Outline each Plasmodium malariae-infected red blood cell.
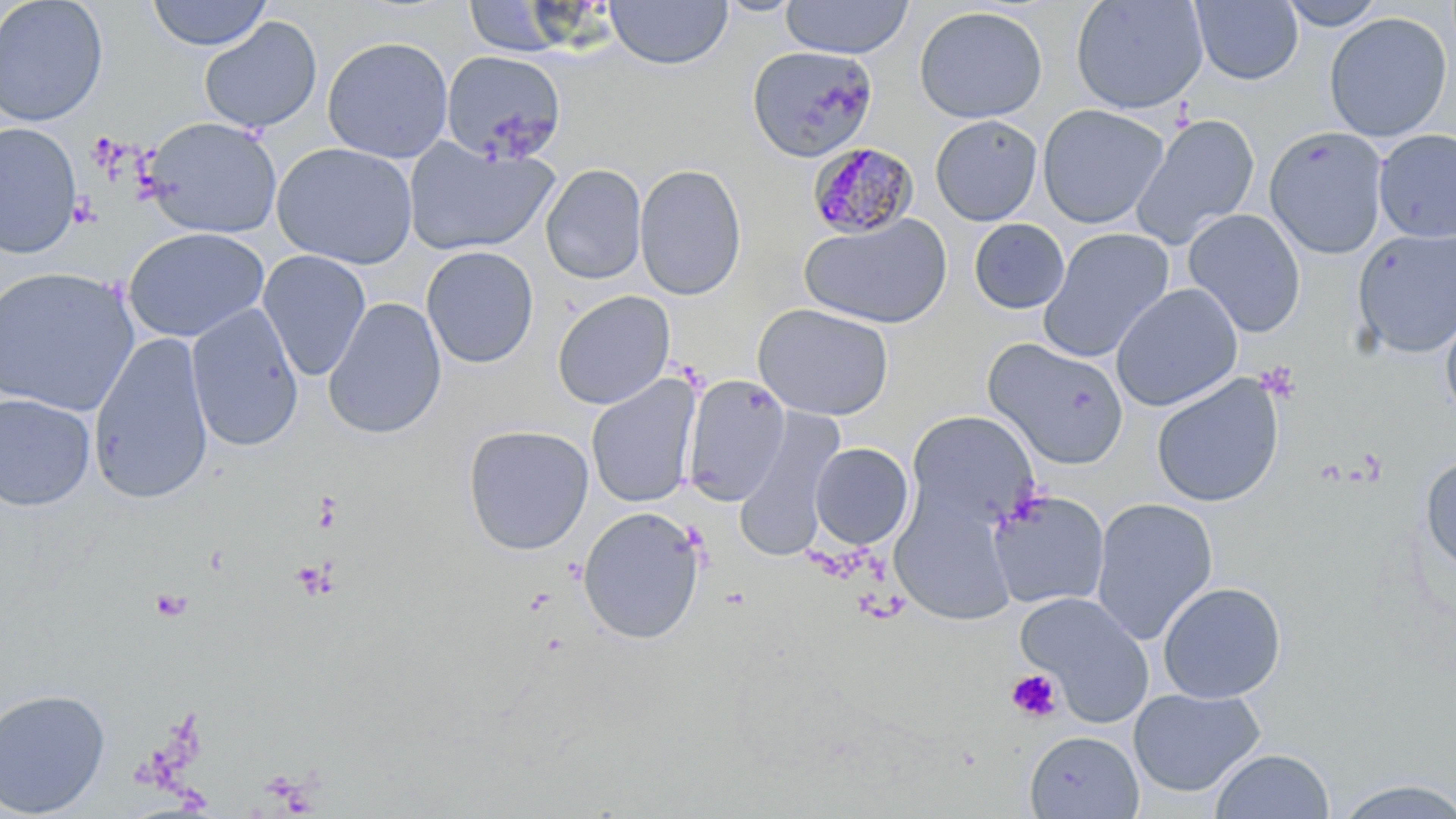

Approximate bounding boxes as [x1, y1, x2, y2] in pixels.
Plasmodium malariae-infected red blood cells: [807, 141, 918, 239].

slide-level diagnosis = Plasmodium malariae
modality = optical microscopy
stain = May-Grünwald-Giemsa
image size = 1456×819 pixels
uninfected red blood cell locations = approximate bounding boxes as [x1, y1, x2, y2] in pixels: [0, 0, 109, 127], [605, 0, 732, 69], [715, 0, 805, 17], [780, 0, 914, 59], [1070, 0, 1209, 114], [1190, 0, 1303, 85], [1277, 0, 1389, 30], [145, 1, 273, 51], [463, 1, 572, 57], [914, 5, 1048, 123], [1323, 12, 1453, 143], [198, 16, 323, 135], [321, 36, 454, 163], [747, 45, 878, 163], [440, 51, 567, 163], [1037, 104, 1170, 229], [1130, 113, 1260, 251], [930, 114, 1043, 226], [142, 116, 282, 239], [0, 122, 83, 259], [1265, 127, 1389, 259], [1373, 128, 1456, 244], [403, 138, 559, 256], [271, 143, 418, 269], [541, 163, 647, 285], [634, 163, 746, 300], [1183, 209, 1307, 337], [800, 213, 953, 329], [968, 219, 1070, 314], [123, 227, 270, 343], [1038, 227, 1175, 363], [1352, 228, 1456, 359], [421, 246, 539, 369], [258, 250, 371, 381], [0, 267, 141, 418], [1110, 282, 1242, 412], [551, 290, 676, 410], [323, 297, 447, 439], [186, 302, 304, 452], [752, 303, 894, 420], [1440, 303, 1456, 425], [88, 333, 214, 504], [983, 338, 1129, 470], [585, 374, 702, 509], [683, 374, 789, 505], [1150, 374, 1285, 508], [0, 393, 96, 511], [734, 407, 845, 563], [906, 409, 1040, 531], [462, 424, 594, 556], [810, 442, 913, 549], [1420, 454, 1456, 576], [988, 490, 1110, 610], [891, 493, 1016, 626], [1090, 496, 1218, 645], [577, 506, 706, 644], [1157, 581, 1286, 704], [1015, 591, 1154, 724], [1128, 687, 1266, 797], [0, 688, 112, 817], [1024, 730, 1144, 818], [1208, 748, 1335, 819], [1331, 777, 1456, 819]
platelet locations = approximate bounding boxes as [x1, y1, x2, y2] in pixels: [1257, 362, 1301, 402], [312, 493, 342, 533], [290, 559, 337, 601], [150, 588, 193, 622], [1005, 668, 1063, 723]
field of view = single
preparation = thin blood film
magnification = 1000x